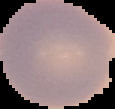
Malaria status: uninfected. Segmented cell region on a black background. Image is 115×109 pixels. From a thin blood smear.